Outline each Plasmodium falciparum-infected red blood cell.
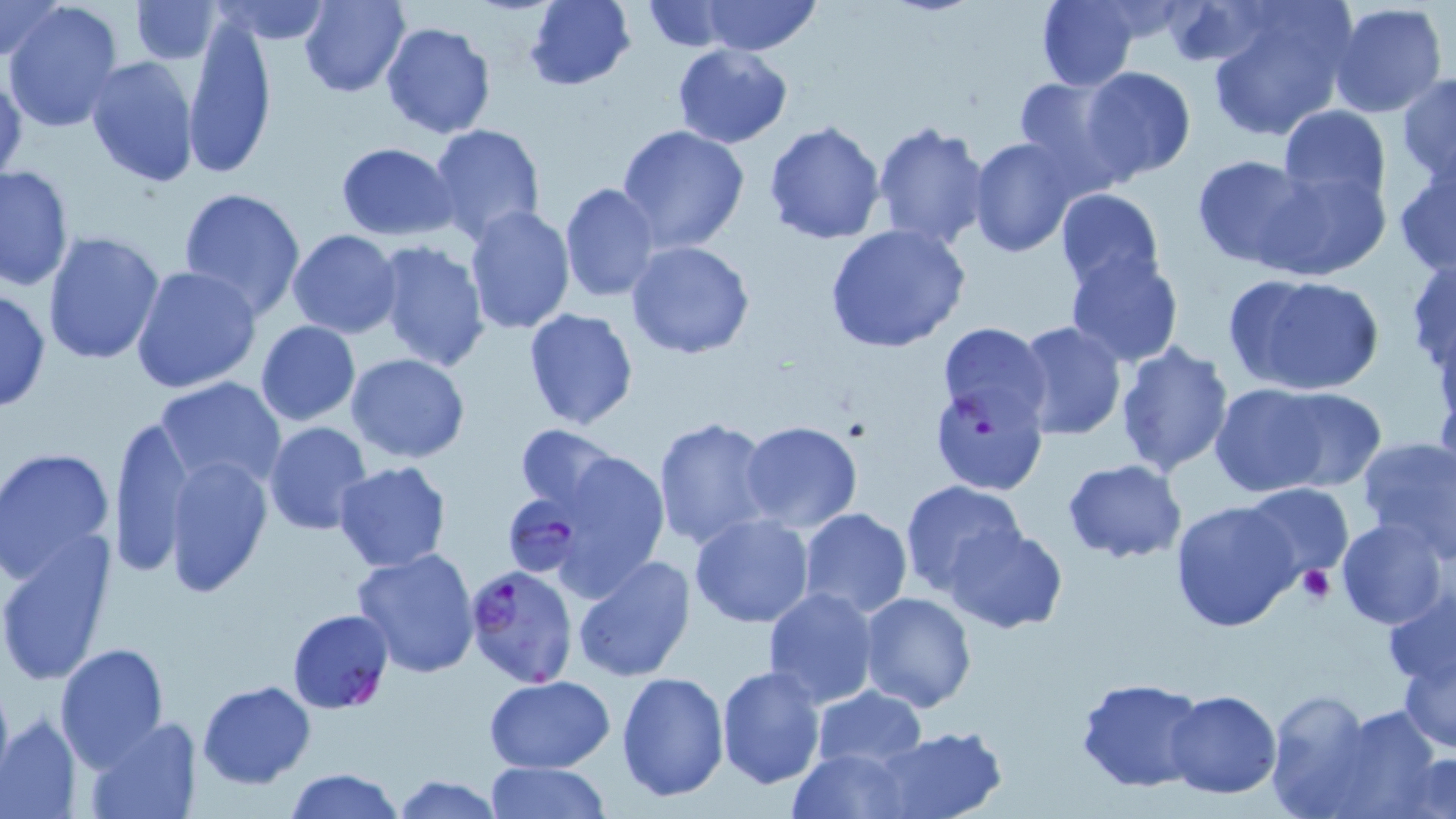

Approximate bounding boxes as [x1, y1, x2, y2] in pixels.
Plasmodium falciparum-infected red blood cells: [937, 322, 1052, 436], [504, 496, 593, 590], [465, 563, 579, 688], [287, 608, 394, 715].

Summary:
  - Platelet locations: [1297, 565, 1334, 606]
  - Uninfected red blood cell locations: [210, 0, 335, 44], [298, 0, 412, 97], [524, 0, 635, 90], [701, 0, 820, 56], [1036, 0, 1139, 90], [1163, 0, 1273, 70], [0, 1, 64, 65], [132, 1, 223, 64], [2, 2, 124, 134], [642, 2, 735, 51], [1328, 2, 1448, 118], [1201, 4, 1354, 142], [182, 14, 279, 179], [378, 20, 497, 142], [672, 43, 792, 148], [84, 56, 199, 188], [1084, 66, 1195, 182], [0, 69, 27, 187], [1397, 73, 1456, 184], [1011, 74, 1132, 190], [1277, 104, 1390, 210], [763, 120, 887, 244], [872, 120, 991, 251], [429, 123, 545, 243], [615, 123, 749, 254], [968, 135, 1084, 258], [336, 143, 457, 239], [1191, 154, 1315, 269], [1392, 158, 1456, 275], [1, 162, 74, 292], [1255, 167, 1391, 281], [558, 182, 660, 302], [178, 186, 306, 320], [1054, 187, 1165, 291], [463, 205, 575, 334], [824, 225, 971, 354], [288, 229, 402, 339], [41, 230, 165, 366], [624, 238, 756, 360], [370, 241, 490, 373], [1406, 248, 1455, 380], [1064, 251, 1185, 369], [130, 265, 261, 394], [1223, 270, 1386, 396], [0, 287, 50, 414], [521, 307, 638, 430], [255, 321, 361, 426], [1011, 322, 1128, 441], [1114, 341, 1236, 477], [346, 353, 470, 462], [154, 377, 288, 495], [1209, 385, 1351, 497], [1270, 386, 1383, 491], [931, 387, 1047, 494], [109, 410, 196, 578], [652, 417, 774, 548], [738, 420, 865, 534], [263, 422, 372, 536], [514, 423, 620, 513], [1354, 435, 1456, 558], [0, 447, 116, 583], [547, 448, 670, 596], [163, 455, 272, 597], [1061, 459, 1185, 564], [334, 461, 451, 571], [899, 480, 1028, 596], [1241, 483, 1353, 584], [1170, 499, 1303, 634], [797, 508, 914, 620], [689, 513, 816, 627], [1335, 518, 1451, 632], [943, 523, 1068, 634], [0, 534, 118, 684], [351, 548, 482, 680], [572, 554, 695, 682], [1381, 583, 1456, 689], [761, 586, 881, 709], [859, 592, 976, 712], [55, 642, 171, 769], [1397, 646, 1456, 754], [715, 664, 826, 790], [616, 671, 729, 802], [484, 676, 615, 773], [1075, 677, 1207, 792], [196, 681, 316, 788], [1263, 685, 1383, 819], [812, 686, 926, 772], [1164, 688, 1282, 799], [1294, 698, 1449, 818], [1, 713, 84, 818], [81, 715, 204, 819], [872, 726, 1008, 819], [790, 748, 913, 819], [1403, 752, 1456, 819], [481, 762, 615, 818], [285, 767, 404, 819], [390, 775, 505, 818]
  - Slide-level diagnosis: Plasmodium falciparum
  - Field of view: single
  - Stain: May-Grünwald-Giemsa
  - Preparation: thin blood smear
  - Modality: light microscopy
  - Image size: 1456×819 pixels
  - Magnification: 1000x